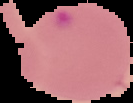

image type = segmented cell region with the area outside set to black
image size = 133×103 pixels
malaria status = parasitized
preparation = thin blood smear